Locate every Plasmodium vivax-infected red blood cell.
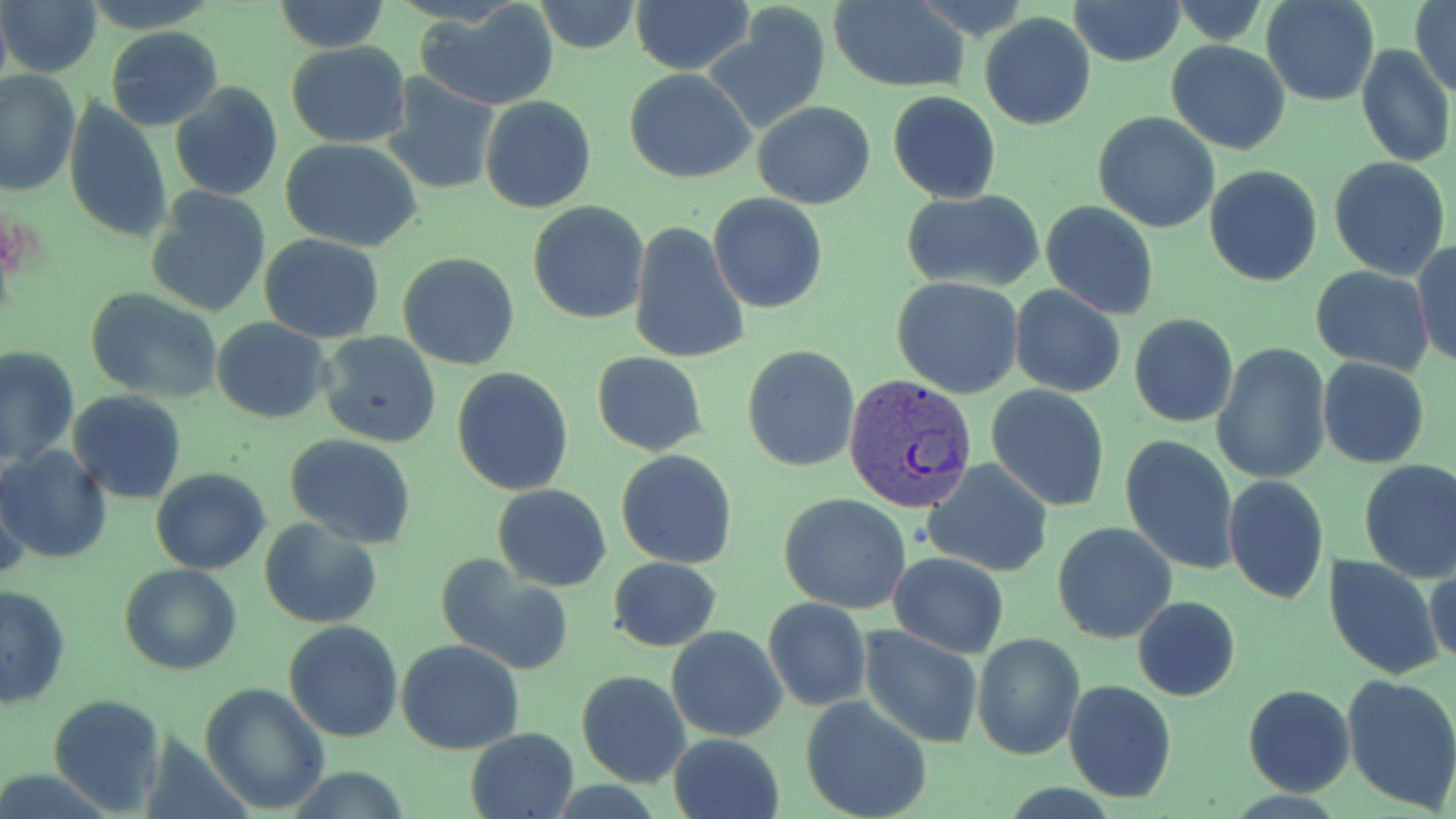

Approximate bounding boxes as [x1, y1, x2, y2] in pixels.
Plasmodium vivax-infected red blood cells: [845, 374, 981, 515].

slide_level_diagnosis: Plasmodium vivax
field_of_view: single
preparation: thin blood film
modality: light microscopy
stain: May-Grünwald-Giemsa
image_size: 1456×819 pixels
magnification: 1000x
uninfected_red_blood_cell_locations: 'approximate bounding boxes as [x1, y1, x2, y2] in pixels: [2, 0, 103, 79], [630, 0, 755, 73], [1067, 0, 1184, 66], [1261, 0, 1379, 107], [1411, 0, 1456, 98], [275, 1, 390, 53], [415, 1, 561, 111], [534, 1, 639, 54], [829, 1, 967, 92], [1165, 4, 1273, 43], [707, 7, 832, 134], [979, 12, 1097, 129], [105, 27, 224, 131], [1166, 39, 1291, 154], [285, 41, 411, 148], [1356, 43, 1454, 168], [625, 69, 756, 184], [1, 71, 79, 196], [383, 77, 501, 193], [170, 84, 283, 202], [887, 92, 1001, 204], [480, 96, 597, 215], [62, 99, 172, 242], [752, 102, 876, 209], [1092, 111, 1221, 231], [281, 139, 424, 252], [1328, 156, 1451, 279], [1204, 165, 1323, 286], [144, 188, 270, 318], [901, 189, 1046, 293], [708, 193, 828, 312], [1041, 201, 1159, 318], [529, 202, 651, 323], [628, 220, 749, 367], [258, 234, 385, 343], [1413, 240, 1455, 370], [397, 252, 522, 370], [1310, 266, 1433, 373], [892, 276, 1024, 399], [1009, 286, 1126, 399], [84, 287, 223, 405], [1128, 314, 1238, 428], [210, 319, 332, 423], [319, 330, 442, 448], [741, 344, 860, 472], [0, 345, 79, 465], [1212, 345, 1331, 485], [592, 352, 707, 457], [1318, 358, 1431, 469], [452, 367, 574, 496], [985, 384, 1111, 511], [67, 391, 186, 503], [1119, 434, 1240, 575], [285, 435, 417, 548], [0, 445, 113, 563], [616, 449, 739, 568], [922, 459, 1055, 576], [1358, 459, 1456, 583], [152, 468, 271, 575], [1223, 474, 1330, 603], [1, 477, 31, 587], [494, 484, 611, 590], [779, 492, 912, 612], [259, 518, 382, 627], [1052, 520, 1178, 644], [434, 553, 573, 676], [888, 553, 1011, 657], [1324, 555, 1444, 681], [609, 556, 722, 652], [119, 564, 241, 675], [1424, 564, 1456, 669], [0, 583, 71, 708], [1132, 595, 1240, 701], [763, 597, 872, 711], [284, 620, 404, 743], [666, 625, 788, 743], [859, 625, 983, 748], [972, 632, 1084, 759], [396, 638, 524, 754], [576, 670, 690, 788], [1341, 672, 1456, 811], [1063, 679, 1178, 804], [200, 683, 328, 813], [1243, 684, 1356, 797], [47, 693, 168, 814], [800, 696, 933, 819], [465, 727, 580, 819], [668, 733, 787, 819]'